Locate every Plasmodium parasite.
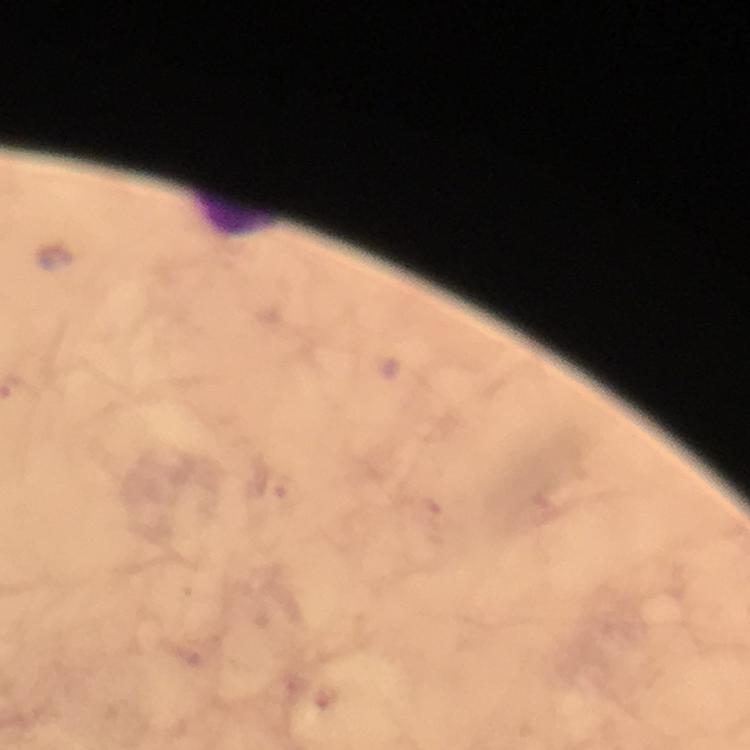

No Plasmodium parasites detected.

{
  "magnification": "100x",
  "leukocyte_locations": "approximate centers as (x, y) in pixels: (236, 217)",
  "image_size": "750×750 pixels",
  "preparation": "thick smear",
  "cropped_from": "a single field of view",
  "capture": "smartphone camera through the microscope",
  "stain": "Giemsa",
  "context": "from a diagnostic examination for malaria",
  "immersion_oil": "applied"
}